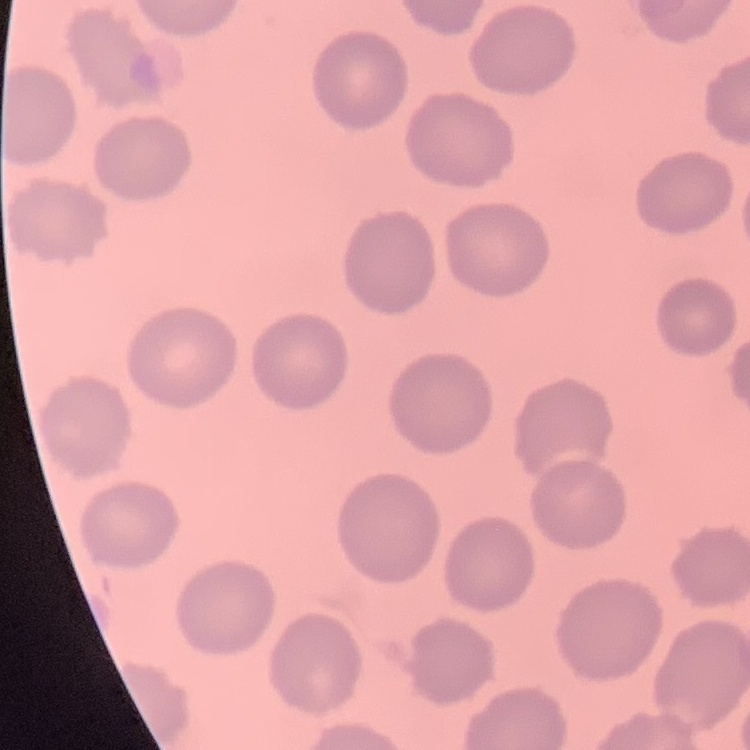
red blood cell morphology = no rouleaux formation
image type = square crop of a larger photomicrograph
stain = Field's or Giemsa
preparation = thin blood smear